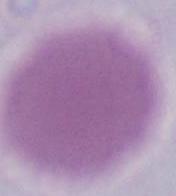
{
  "modality": "photomicrograph",
  "identification": "erythrocyte",
  "magnification": "1000x"
}